Report the malaria status of this cell.
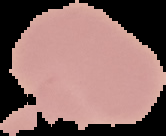
Uninfected.

Image is 166×136 pixels. Segmented cell region on a black background. From a thin blood film.